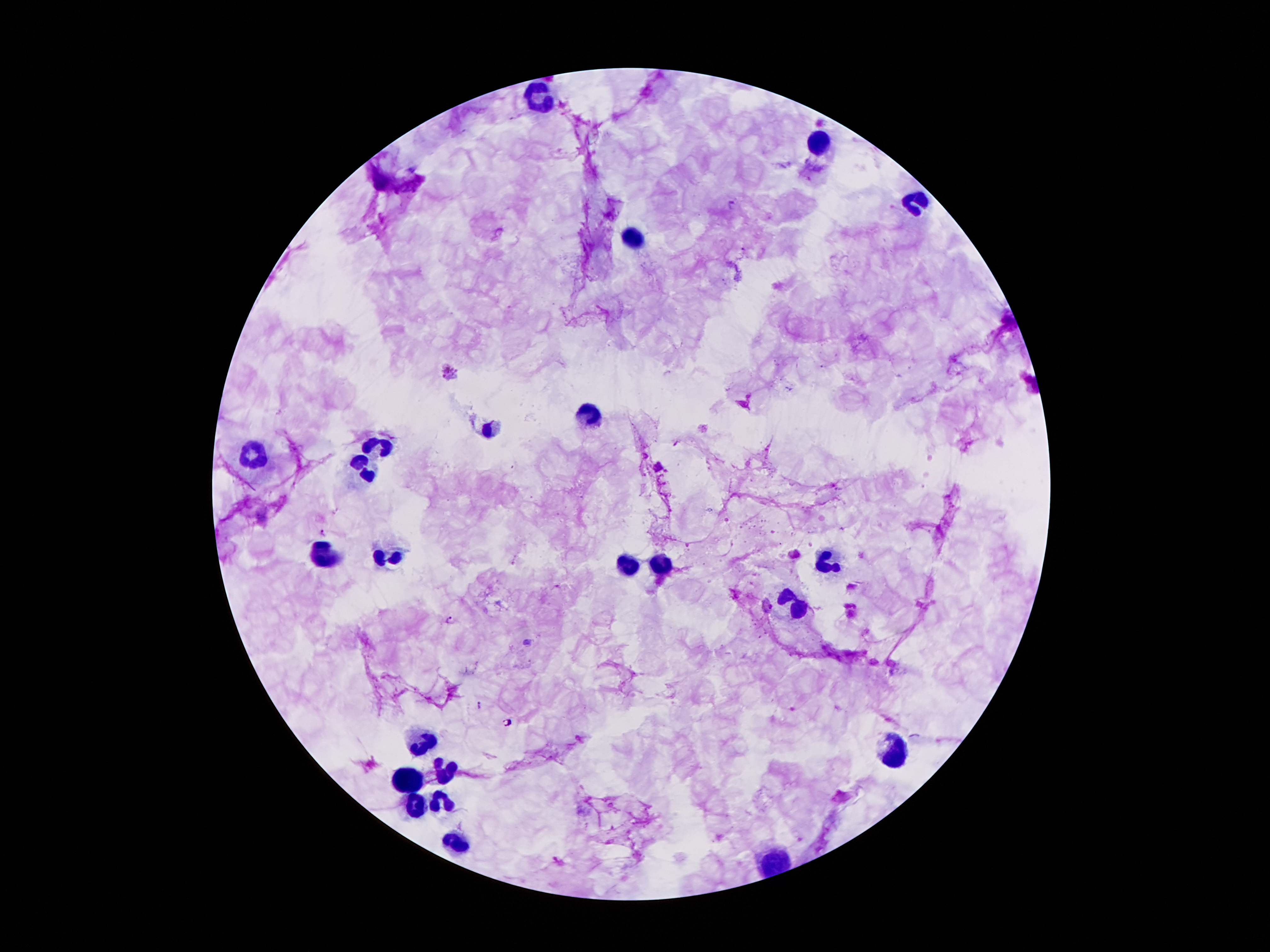
Approximate centers as (x, y) in pixels.
Summary:
  - Plasmodium parasite locations: (731, 205), (451, 375), (322, 532), (453, 621), (479, 705), (508, 723)
  - Leukocyte locations: (543, 95), (820, 142), (914, 203), (634, 238), (590, 413), (489, 433), (387, 445), (254, 455), (367, 472), (323, 554), (387, 556), (825, 559), (624, 566), (659, 569), (800, 608), (422, 742), (899, 747), (447, 771), (407, 778), (444, 803), (414, 805), (456, 838)
  - Field of view: single
  - Preparation: thick peripheral-blood smear
  - Magnification: 100x
  - Patient malaria status: positive for Plasmodium falciparum
  - Stain: Giemsa
  - Capture: smartphone through the microscope eyepiece
  - Image size: 1270×952 pixels